Assess the morphology of the erythrocytes.
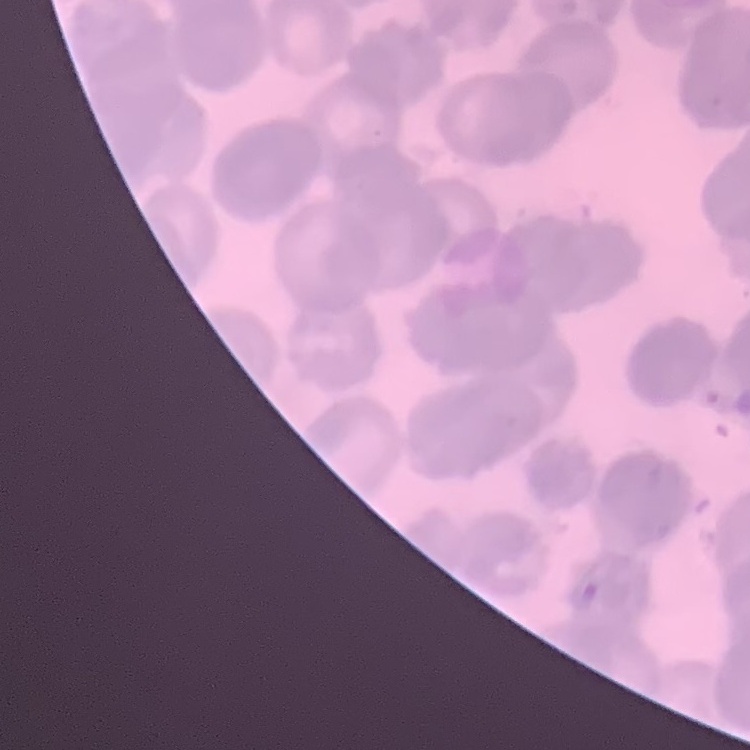

They show rouleaux formation.

Thin blood film. One tile cut from a larger photomicrograph. Field's or Giemsa stain.